Name the parasite shown.
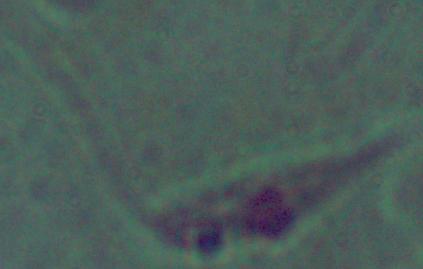

Leishmania.

Micrograph. Captured at 1000x magnification.